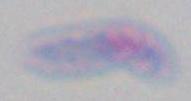
{
  "modality": "photomicrograph",
  "magnification": "1000x",
  "identification": "Toxoplasma gondii"
}